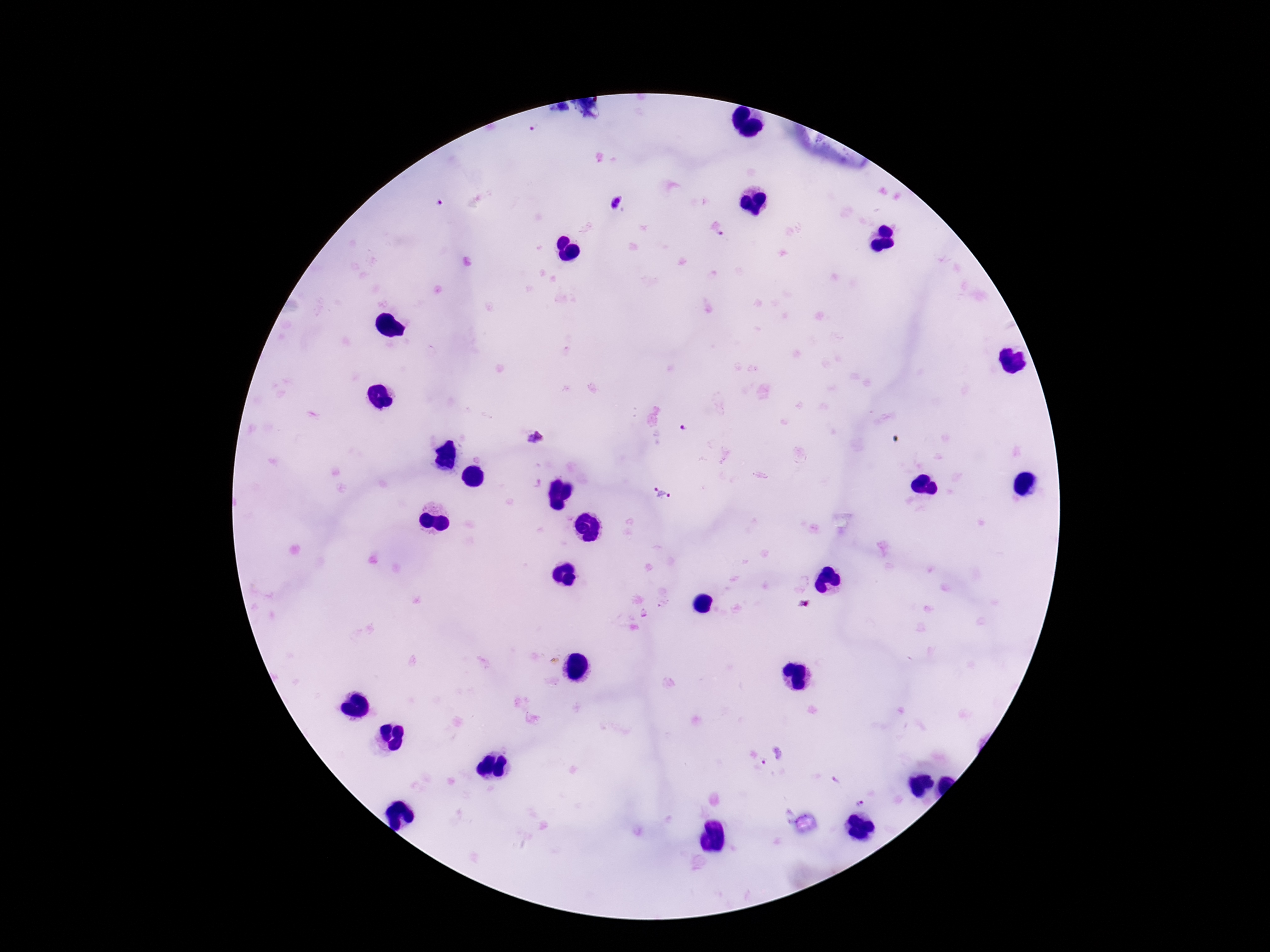

Approximate centers as (x, y) in pixels. Plasmodium parasite locations: (534, 128), (437, 202), (617, 204), (685, 429), (535, 437), (663, 492), (765, 761), (860, 801). Thick blood smear. Smartphone photograph taken through the microscope eyepiece. Patient malaria status: infected. Image is 1270×952 pixels. Giemsa stain. 100x magnification. One field from this slide.